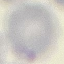
Malaria status: uninfected. Thin smear of blood. Giemsa-stained preparation. Photographed with a smartphone camera at the microscope eyepiece. Automatically extracted cell patch, resized to 64 × 64 pixels.